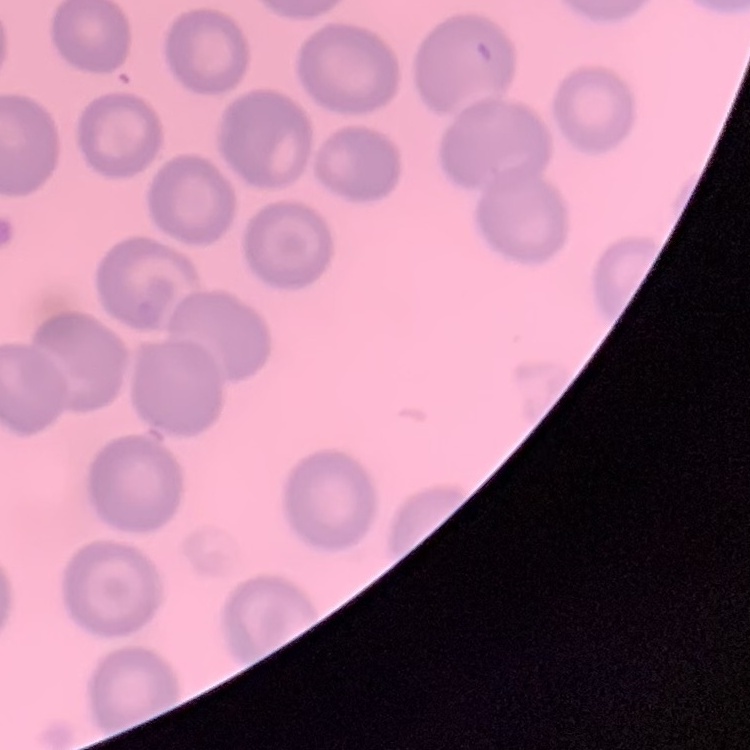

erythrocyte morphology = no rouleaux formation
stain = Field's or Giemsa
preparation = thin blood smear
image type = square crop of a larger photomicrograph